Point out leukocytes.
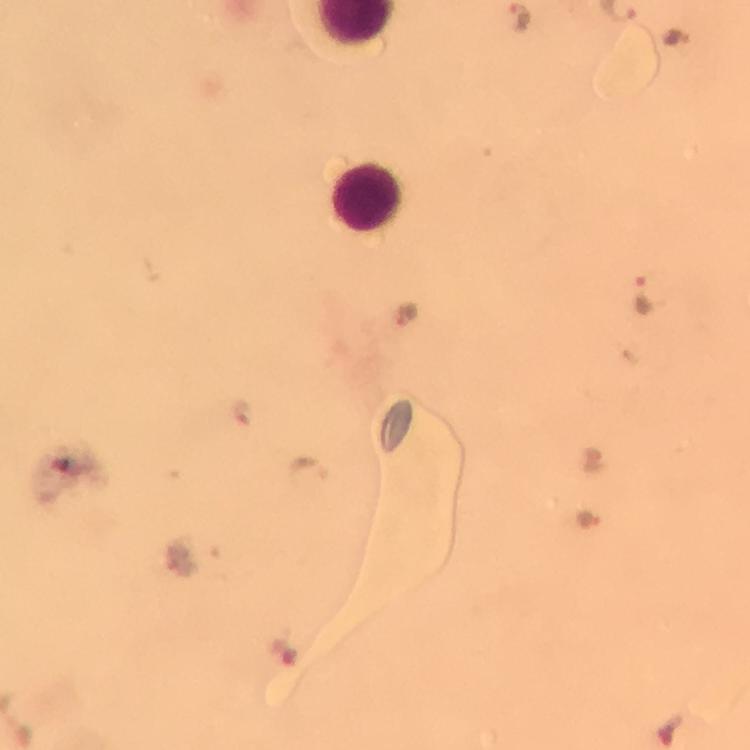
Approximate centers as {x, y} in pixels.
Leukocytes: {369, 199}.

Summary:
  - Plasmodium parasite locations: {521, 16}, {672, 38}, {641, 293}, {407, 318}, {243, 414}, {309, 471}, {590, 522}
  - Image size: 750×750 pixels
  - Magnification: 100x
  - Capture: smartphone camera through the microscope
  - Cropped from: one field of view
  - Stain: Giemsa
  - Immersion oil: applied
  - Context: from a malaria diagnostic workup
  - Preparation: thick blood smear